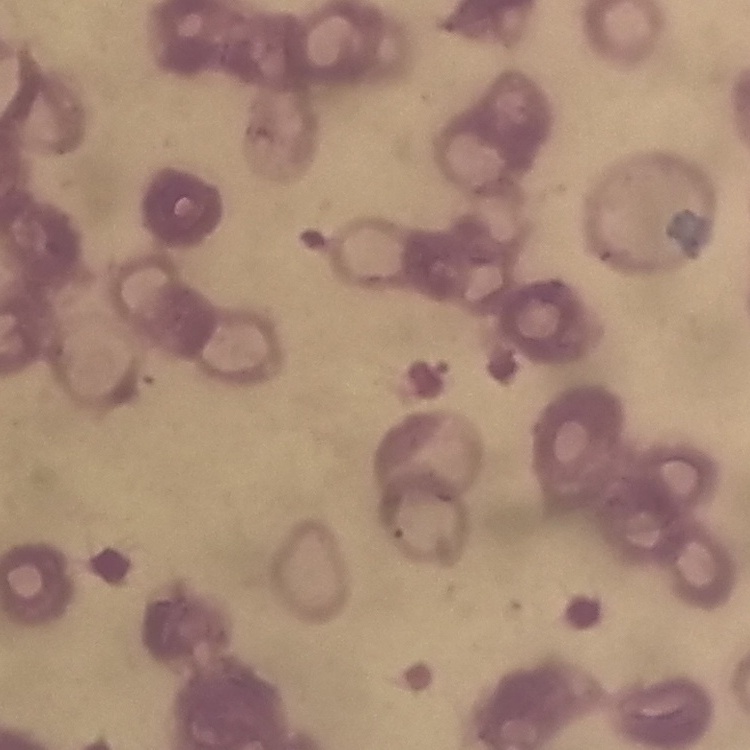
red blood cell morphology = rouleaux formation
stain = Field's or Giemsa
image type = square crop of a larger photomicrograph
preparation = thin blood film